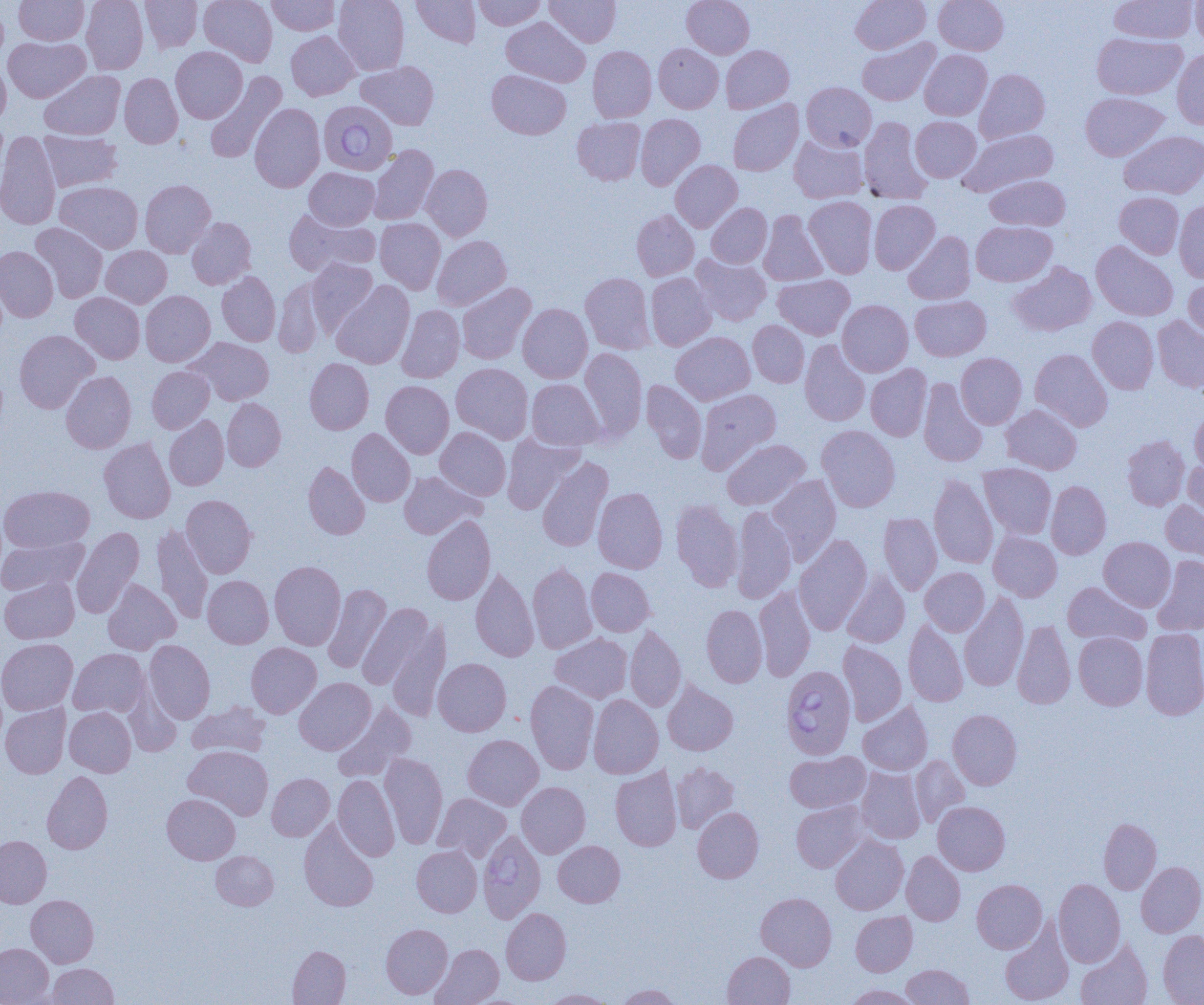
slide-level diagnosis = Babesia divergens
uninfected red blood cell locations = approximate bounding boxes as named x1/y1/x2/y2 corners in pixels: (x1=14, y1=0, x2=89, y2=45), (x1=81, y1=0, x2=148, y2=75), (x1=140, y1=0, x2=202, y2=52), (x1=199, y1=0, x2=277, y2=67), (x1=266, y1=0, x2=341, y2=35), (x1=333, y1=0, x2=409, y2=75), (x1=412, y1=0, x2=480, y2=47), (x1=473, y1=0, x2=546, y2=30), (x1=545, y1=0, x2=621, y2=47), (x1=682, y1=0, x2=754, y2=58), (x1=851, y1=0, x2=931, y2=54), (x1=934, y1=0, x2=1008, y2=55), (x1=1110, y1=0, x2=1197, y2=43), (x1=1191, y1=1, x2=1204, y2=48), (x1=0, y1=2, x2=9, y2=69), (x1=501, y1=17, x2=590, y2=87), (x1=286, y1=31, x2=359, y2=101), (x1=1092, y1=33, x2=1187, y2=99), (x1=3, y1=37, x2=90, y2=102), (x1=857, y1=38, x2=939, y2=106), (x1=654, y1=43, x2=723, y2=113), (x1=721, y1=45, x2=794, y2=113), (x1=171, y1=46, x2=247, y2=123), (x1=588, y1=46, x2=656, y2=122), (x1=1172, y1=49, x2=1204, y2=130), (x1=920, y1=50, x2=992, y2=120), (x1=0, y1=60, x2=11, y2=128), (x1=356, y1=61, x2=439, y2=130), (x1=975, y1=69, x2=1050, y2=143), (x1=40, y1=70, x2=125, y2=140), (x1=487, y1=70, x2=571, y2=139), (x1=204, y1=72, x2=287, y2=163), (x1=119, y1=73, x2=183, y2=148), (x1=802, y1=82, x2=876, y2=151), (x1=1080, y1=93, x2=1168, y2=161), (x1=728, y1=100, x2=803, y2=176), (x1=249, y1=103, x2=325, y2=192), (x1=636, y1=114, x2=705, y2=190), (x1=859, y1=116, x2=932, y2=204), (x1=910, y1=116, x2=981, y2=182), (x1=572, y1=117, x2=645, y2=185), (x1=959, y1=129, x2=1059, y2=196), (x1=1120, y1=130, x2=1204, y2=199), (x1=0, y1=132, x2=61, y2=230), (x1=39, y1=132, x2=122, y2=191), (x1=789, y1=134, x2=869, y2=204), (x1=369, y1=145, x2=439, y2=225), (x1=671, y1=160, x2=742, y2=232), (x1=421, y1=164, x2=492, y2=241), (x1=304, y1=168, x2=379, y2=229), (x1=984, y1=175, x2=1070, y2=231), (x1=139, y1=180, x2=216, y2=257), (x1=55, y1=181, x2=143, y2=253), (x1=1114, y1=192, x2=1184, y2=258), (x1=804, y1=196, x2=877, y2=278), (x1=869, y1=200, x2=940, y2=274), (x1=1174, y1=201, x2=1204, y2=283), (x1=706, y1=203, x2=772, y2=268), (x1=284, y1=209, x2=380, y2=276), (x1=631, y1=210, x2=699, y2=281), (x1=758, y1=210, x2=827, y2=286), (x1=186, y1=217, x2=256, y2=289), (x1=375, y1=218, x2=446, y2=293), (x1=971, y1=221, x2=1056, y2=286), (x1=30, y1=223, x2=108, y2=303), (x1=903, y1=231, x2=975, y2=304), (x1=432, y1=235, x2=511, y2=310), (x1=1091, y1=240, x2=1178, y2=321), (x1=0, y1=246, x2=58, y2=322), (x1=101, y1=246, x2=171, y2=308), (x1=691, y1=254, x2=771, y2=326), (x1=306, y1=258, x2=377, y2=335), (x1=1008, y1=262, x2=1096, y2=336), (x1=217, y1=271, x2=280, y2=346), (x1=580, y1=272, x2=656, y2=354), (x1=645, y1=273, x2=715, y2=351), (x1=773, y1=274, x2=854, y2=339), (x1=1183, y1=274, x2=1204, y2=342), (x1=274, y1=278, x2=326, y2=358), (x1=332, y1=281, x2=414, y2=369), (x1=457, y1=283, x2=536, y2=364), (x1=140, y1=290, x2=215, y2=366), (x1=70, y1=292, x2=145, y2=364), (x1=910, y1=295, x2=991, y2=361), (x1=837, y1=300, x2=913, y2=376), (x1=518, y1=303, x2=592, y2=383), (x1=396, y1=305, x2=464, y2=383), (x1=1087, y1=316, x2=1158, y2=394), (x1=1152, y1=316, x2=1204, y2=392), (x1=748, y1=321, x2=809, y2=387), (x1=14, y1=330, x2=99, y2=413), (x1=671, y1=332, x2=755, y2=405), (x1=187, y1=337, x2=274, y2=406), (x1=800, y1=340, x2=870, y2=426), (x1=579, y1=348, x2=647, y2=441), (x1=1030, y1=349, x2=1113, y2=431), (x1=956, y1=353, x2=1027, y2=429), (x1=305, y1=358, x2=374, y2=434), (x1=451, y1=363, x2=533, y2=443), (x1=866, y1=364, x2=932, y2=441), (x1=147, y1=366, x2=214, y2=433), (x1=61, y1=371, x2=136, y2=453), (x1=918, y1=378, x2=988, y2=467), (x1=527, y1=379, x2=604, y2=450), (x1=641, y1=380, x2=707, y2=463), (x1=381, y1=381, x2=454, y2=459), (x1=695, y1=388, x2=781, y2=474), (x1=222, y1=398, x2=286, y2=471), (x1=1001, y1=404, x2=1081, y2=474), (x1=1190, y1=407, x2=1204, y2=475), (x1=164, y1=415, x2=228, y2=490), (x1=817, y1=425, x2=900, y2=512), (x1=436, y1=427, x2=511, y2=500), (x1=347, y1=428, x2=415, y2=506), (x1=502, y1=434, x2=585, y2=513), (x1=1122, y1=435, x2=1189, y2=510), (x1=99, y1=438, x2=175, y2=523), (x1=721, y1=438, x2=810, y2=510), (x1=537, y1=457, x2=613, y2=552), (x1=303, y1=461, x2=370, y2=539), (x1=1183, y1=461, x2=1204, y2=528), (x1=979, y1=463, x2=1056, y2=539), (x1=399, y1=472, x2=485, y2=538), (x1=929, y1=473, x2=998, y2=569), (x1=767, y1=475, x2=841, y2=564), (x1=1046, y1=480, x2=1111, y2=559), (x1=0, y1=485, x2=95, y2=553), (x1=593, y1=487, x2=668, y2=573), (x1=181, y1=494, x2=257, y2=578), (x1=671, y1=499, x2=743, y2=592), (x1=1161, y1=500, x2=1204, y2=564), (x1=731, y1=505, x2=797, y2=603), (x1=879, y1=513, x2=941, y2=595), (x1=422, y1=515, x2=496, y2=605), (x1=152, y1=524, x2=213, y2=624), (x1=71, y1=527, x2=144, y2=618), (x1=988, y1=531, x2=1061, y2=601), (x1=794, y1=535, x2=872, y2=635), (x1=0, y1=536, x2=88, y2=596), (x1=1099, y1=537, x2=1175, y2=611), (x1=1152, y1=556, x2=1204, y2=635), (x1=269, y1=560, x2=345, y2=650), (x1=528, y1=563, x2=596, y2=653), (x1=470, y1=567, x2=539, y2=662), (x1=920, y1=567, x2=989, y2=636), (x1=586, y1=568, x2=655, y2=636), (x1=841, y1=571, x2=910, y2=648), (x1=202, y1=575, x2=273, y2=648), (x1=0, y1=576, x2=80, y2=644), (x1=102, y1=579, x2=180, y2=654), (x1=1063, y1=582, x2=1149, y2=645), (x1=323, y1=583, x2=391, y2=674), (x1=754, y1=585, x2=816, y2=681), (x1=959, y1=592, x2=1028, y2=691), (x1=357, y1=602, x2=434, y2=690), (x1=701, y1=604, x2=767, y2=688), (x1=903, y1=619, x2=968, y2=707), (x1=388, y1=620, x2=450, y2=721), (x1=1012, y1=620, x2=1075, y2=709), (x1=625, y1=625, x2=686, y2=712), (x1=1141, y1=628, x2=1204, y2=720), (x1=550, y1=633, x2=633, y2=703), (x1=1074, y1=633, x2=1147, y2=710), (x1=0, y1=638, x2=78, y2=716), (x1=144, y1=640, x2=215, y2=724), (x1=838, y1=641, x2=906, y2=726), (x1=246, y1=642, x2=321, y2=718), (x1=69, y1=648, x2=149, y2=718), (x1=433, y1=658, x2=511, y2=736), (x1=294, y1=678, x2=375, y2=755), (x1=525, y1=680, x2=598, y2=774), (x1=663, y1=681, x2=738, y2=755), (x1=588, y1=694, x2=663, y2=779), (x1=858, y1=701, x2=933, y2=775), (x1=187, y1=702, x2=270, y2=757), (x1=0, y1=703, x2=71, y2=778), (x1=333, y1=703, x2=416, y2=782), (x1=64, y1=707, x2=136, y2=776), (x1=948, y1=709, x2=1022, y2=789), (x1=463, y1=734, x2=543, y2=810), (x1=183, y1=745, x2=273, y2=819), (x1=785, y1=751, x2=870, y2=813), (x1=380, y1=753, x2=448, y2=849), (x1=910, y1=755, x2=969, y2=827), (x1=670, y1=762, x2=740, y2=833), (x1=610, y1=766, x2=682, y2=851), (x1=856, y1=767, x2=926, y2=843), (x1=42, y1=771, x2=112, y2=854), (x1=267, y1=773, x2=334, y2=841), (x1=333, y1=775, x2=399, y2=861), (x1=516, y1=782, x2=590, y2=858), (x1=433, y1=793, x2=511, y2=862), (x1=162, y1=794, x2=240, y2=864), (x1=791, y1=801, x2=867, y2=872), (x1=933, y1=801, x2=1010, y2=875), (x1=693, y1=807, x2=763, y2=883), (x1=1099, y1=818, x2=1161, y2=894), (x1=299, y1=820, x2=378, y2=911), (x1=830, y1=835, x2=908, y2=914), (x1=0, y1=836, x2=51, y2=908), (x1=553, y1=840, x2=625, y2=907), (x1=412, y1=845, x2=482, y2=917), (x1=211, y1=851, x2=278, y2=910), (x1=902, y1=851, x2=965, y2=925), (x1=1136, y1=861, x2=1204, y2=937), (x1=1054, y1=878, x2=1125, y2=967), (x1=972, y1=879, x2=1047, y2=953), (x1=756, y1=892, x2=837, y2=971), (x1=26, y1=894, x2=99, y2=967), (x1=501, y1=908, x2=571, y2=984), (x1=851, y1=911, x2=917, y2=976), (x1=381, y1=923, x2=453, y2=999), (x1=999, y1=923, x2=1074, y2=1005), (x1=1158, y1=930, x2=1204, y2=1004), (x1=1075, y1=939, x2=1152, y2=1005), (x1=0, y1=943, x2=53, y2=1004), (x1=431, y1=944, x2=503, y2=1005), (x1=288, y1=945, x2=351, y2=1004), (x1=723, y1=951, x2=795, y2=1005), (x1=47, y1=963, x2=118, y2=1004), (x1=901, y1=964, x2=973, y2=1004), (x1=615, y1=984, x2=682, y2=1004), (x1=843, y1=985, x2=921, y2=1004), (x1=541, y1=989, x2=615, y2=1004)
magnification = 1000x
image size = 1204×1005 pixels
modality = optical microscopy
Babesia divergens-infected red blood cell locations = approximate bounding boxes as named x1/y1/x2/y2 corners in pixels: (x1=318, y1=100, x2=398, y2=175), (x1=781, y1=665, x2=856, y2=759), (x1=477, y1=829, x2=546, y2=923)
preparation = thin blood film
field of view = single